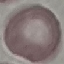

Malaria status: uninfected. Giemsa-stained preparation. Thin smear of blood. Acquired by smartphone through the microscope eyepiece. Cell patch, automatically extracted from a larger field of view and resized to 64 × 64 pixels.